Assess the morphology of the red blood cells.
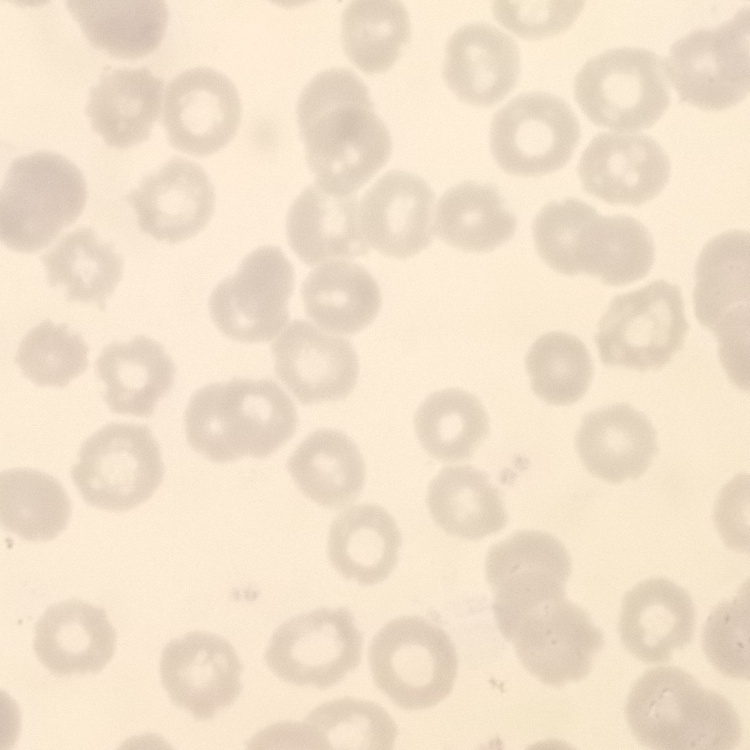
No rouleaux formation.

{
  "image_type": "square crop of a larger photomicrograph",
  "stain": "Field's or Giemsa",
  "preparation": "thin peripheral smear"
}